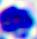

Summary:
  - Modality: photomicrograph
  - Magnification: 400x
  - Identification: leukocyte